Assess this cell for malaria.
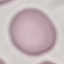
It is uninfected.

Summary:
  - Capture: smartphone through the microscope eyepiece
  - Preparation: thin blood smear
  - Stain: Giemsa
  - Image type: cell patch, automatically extracted from a larger field of view and resized to 64 × 64 pixels